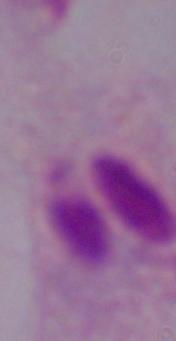
{
  "identification": "trichomonad",
  "magnification": "1000x",
  "modality": "photomicrograph"
}